Point out each malaria parasite.
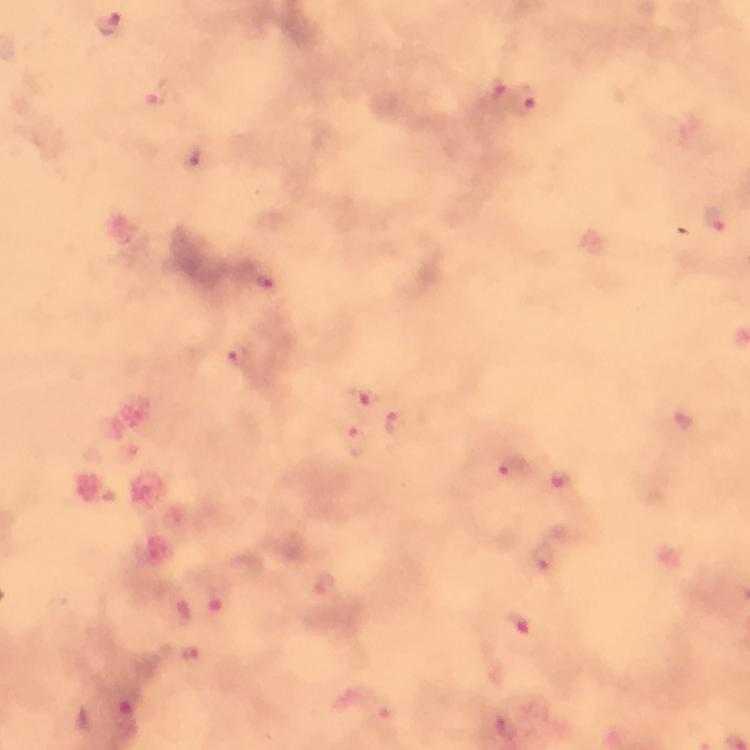
Approximate centers as (x, y) in pixels.
Malaria parasites: (111, 25), (497, 89), (155, 95), (524, 103), (192, 155), (716, 222), (268, 282), (241, 358), (363, 397), (399, 422), (358, 441), (512, 470), (561, 480), (545, 556), (324, 588), (519, 623), (193, 655).

Summary:
  - Context: from a malaria diagnostic workup
  - Magnification: 100x
  - Preparation: thick smear
  - Immersion oil: applied
  - Stain: Giemsa
  - Cropped from: one field of view
  - Capture: smartphone mounted on the microscope
  - Image size: 750×750 pixels